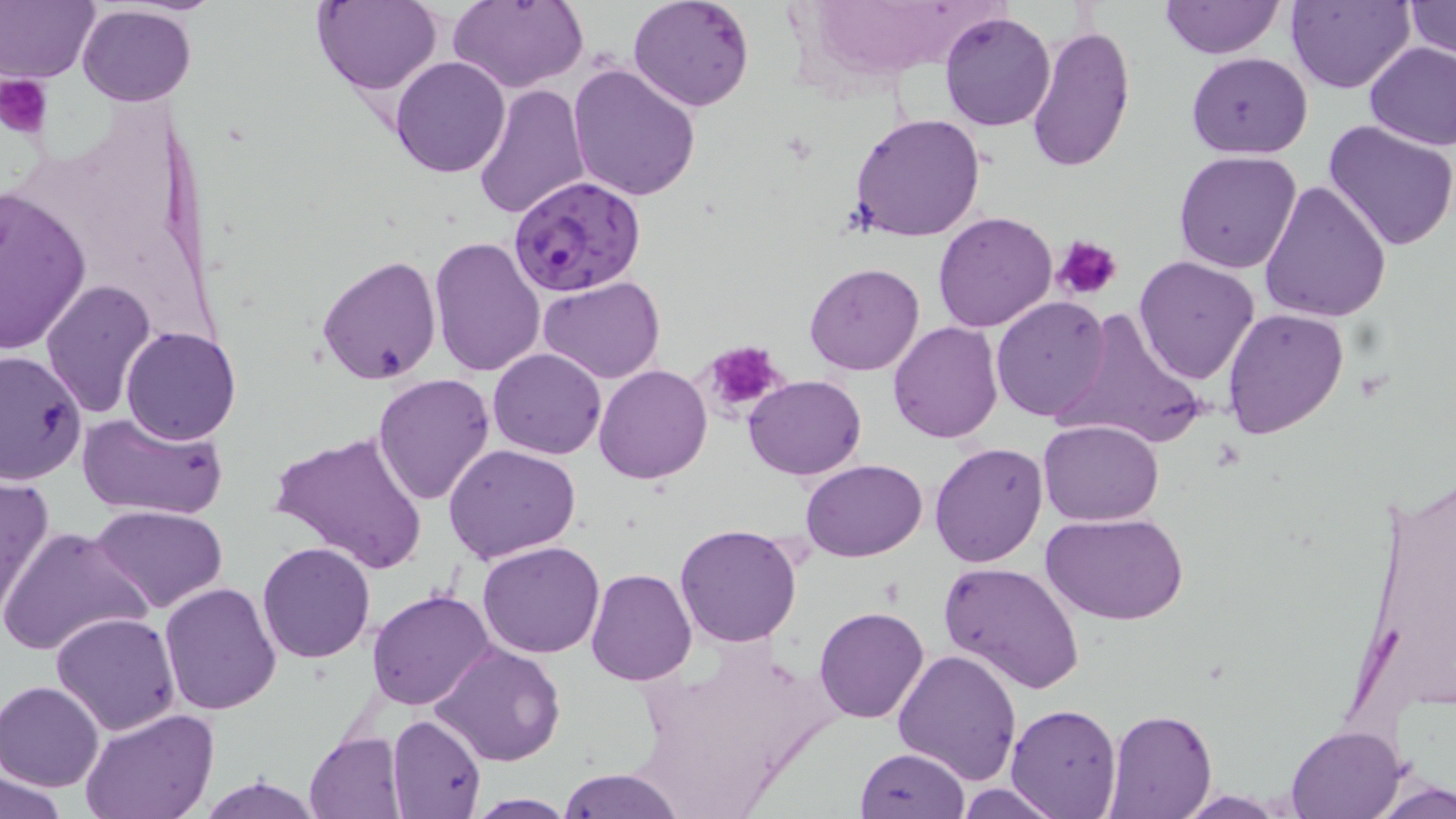
slide_level_diagnosis: Plasmodium falciparum
uninfected_red_blood_cell_locations: 'approximate bounding boxes as (x1,y1)-(x2,y2) corner pairs in pixels: (1,0)-(98,85), (313,0)-(439,95), (448,0)-(586,92), (628,0)-(756,113), (1161,0)-(1283,59), (1286,0)-(1412,95), (1404,2)-(1456,61), (76,5)-(190,109), (940,10)-(1055,132), (1026,23)-(1135,173), (1364,41)-(1456,151), (1186,52)-(1312,159), (390,55)-(511,178), (568,61)-(700,199), (474,84)-(590,221), (848,114)-(988,243), (1323,118)-(1456,252), (1173,150)-(1302,273), (1259,179)-(1390,324), (0,184)-(92,356), (932,211)-(1057,333), (428,236)-(545,378), (317,255)-(443,385), (1133,256)-(1261,385), (804,262)-(924,377), (538,276)-(667,384), (39,280)-(155,416), (991,295)-(1113,422), (1053,307)-(1212,450), (1221,307)-(1349,441), (887,320)-(1003,443), (120,327)-(241,446), (487,349)-(607,459), (0,350)-(87,489), (593,364)-(712,484), (371,373)-(496,507), (743,374)-(866,480), (76,410)-(227,521), (1037,419)-(1164,526), (269,430)-(430,574), (929,443)-(1048,568), (445,444)-(581,564), (800,458)-(929,562), (1353,472)-(1456,723), (0,474)-(54,619), (91,504)-(228,612), (1043,512)-(1188,626), (675,524)-(802,647), (0,525)-(151,658), (478,540)-(604,658), (256,542)-(376,664), (937,561)-(1086,698), (586,568)-(697,687), (159,582)-(281,714), (367,589)-(496,711), (812,606)-(931,724), (50,612)-(181,736), (431,643)-(566,768), (892,647)-(1022,784), (0,681)-(105,791), (1006,703)-(1121,817), (81,710)-(220,819), (1103,710)-(1216,819), (387,714)-(486,819), (1287,724)-(1405,818), (305,733)-(406,819), (854,749)-(969,818), (559,768)-(683,819), (3,769)-(69,819), (196,774)-(322,818), (1371,777)-(1456,819), (953,784)-(1067,818), (466,795)-(580,816)'
plasmodium_falciparum_infected_red_blood_cell_locations: 'approximate bounding boxes as (x1,y1)-(x2,y2) corner pairs in pixels: (509,175)-(647,298)'
field_of_view: one of a larger specimen
magnification: 1000x
preparation: thin blood smear
stain: May-Grünwald-Giemsa
platelet_locations: 'approximate bounding boxes as (x1,y1)-(x2,y2) corner pairs in pixels: (1,76)-(52,135), (1054,235)-(1123,302), (698,340)-(789,419)'
image_size: 1456×819 pixels
modality: light microscopy